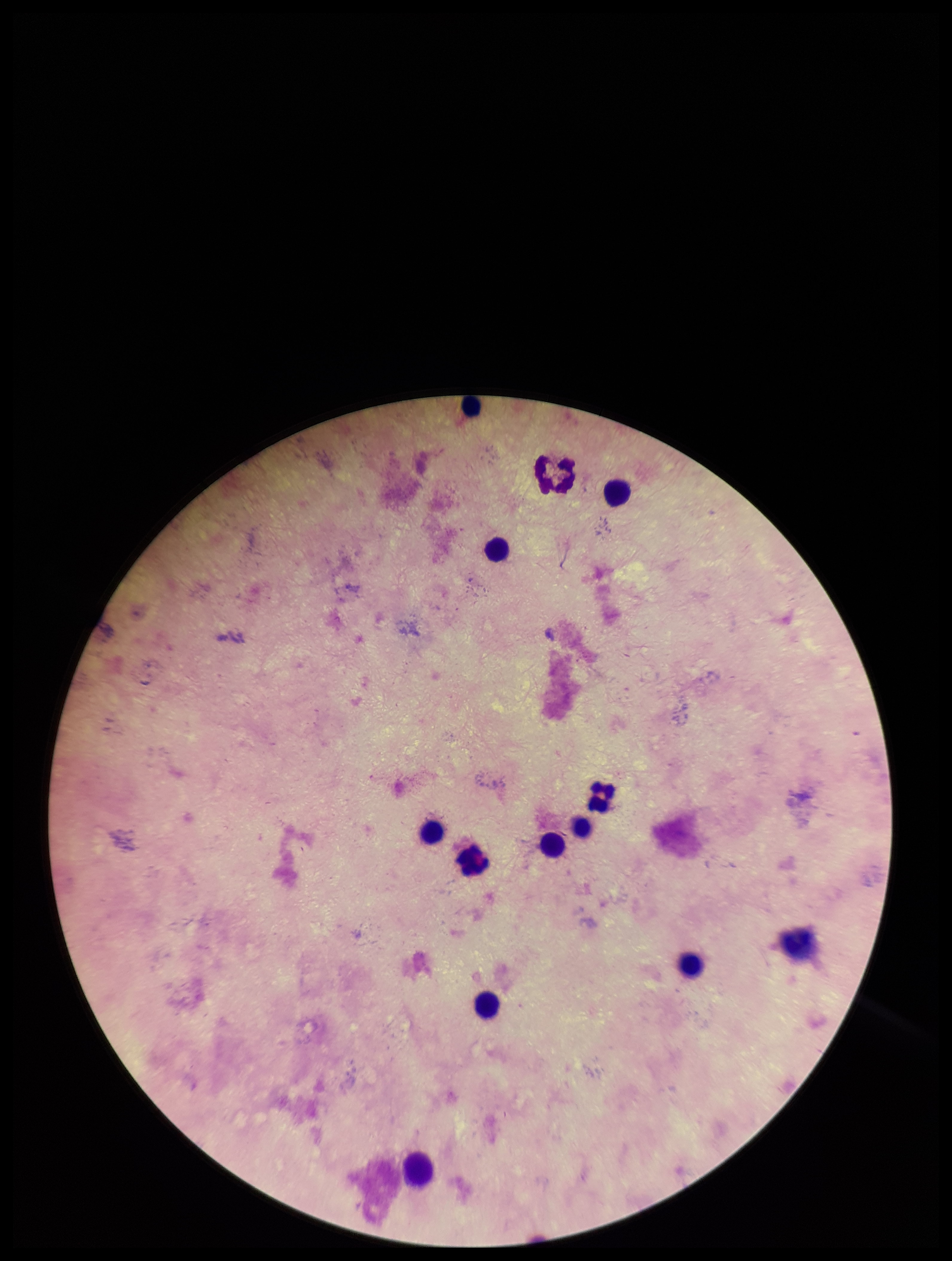

Image is 952×1261 pixels. One field from this slide. Patient malaria status: negative. Giemsa stain. Parasite count: 0. Preparation: thick blood smear. Plasmodium parasites: none seen. Photographed through the microscope eyepiece with a smartphone camera. Leukocyte count: 13.